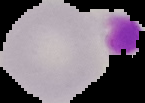 From a thin blood smear. Image is 145×103 pixels. Malaria status: uninfected. Cell region segmented out of the field of view; the surrounding area is masked to black.